Give the extent of all Plasmodium falciparum-infected red blood cells.
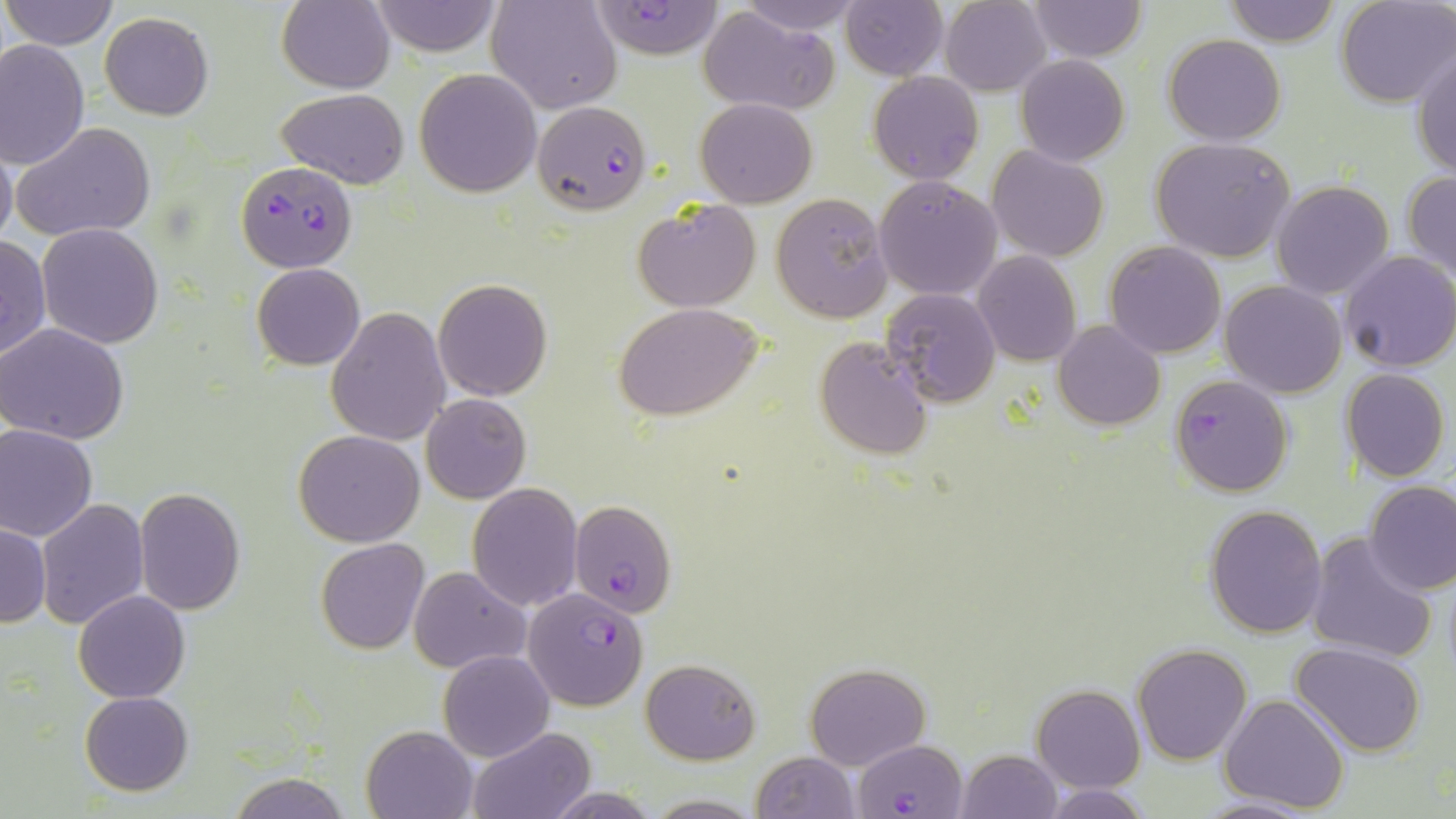

Approximate bounding boxes as (x1,y1)-(x2,y2) corner pairs in pixels.
Plasmodium falciparum-infected red blood cells: (595,0)-(724,61), (530,100)-(652,214), (236,161)-(356,273), (1169,373)-(1294,496), (570,501)-(677,617), (523,587)-(649,711), (855,737)-(971,818).

slide-level diagnosis = Plasmodium falciparum
uninfected red blood cell locations = approximate bounding boxes as (x1,y1)-(x2,y2) corner pairs in pixels: (2,0)-(118,51), (278,0)-(396,93), (487,0)-(623,115), (735,0)-(866,35), (841,0)-(949,80), (940,0)-(1051,95), (1025,0)-(1147,62), (1222,0)-(1342,47), (370,1)-(502,57), (1336,1)-(1454,107), (697,6)-(840,116), (100,12)-(214,120), (1163,34)-(1286,146), (0,39)-(91,172), (1411,47)-(1456,182), (1015,55)-(1131,166), (415,69)-(541,195), (867,71)-(983,184), (278,88)-(408,189), (696,98)-(816,207), (12,122)-(156,242), (0,136)-(17,255), (1151,137)-(1296,262), (987,146)-(1110,262), (1402,173)-(1456,282), (874,177)-(1003,300), (1271,180)-(1395,299), (771,193)-(892,322), (633,198)-(762,312), (38,224)-(164,348), (0,233)-(50,364), (1103,240)-(1229,358), (1336,249)-(1456,372), (973,250)-(1081,366), (253,264)-(365,370), (433,279)-(551,402), (1220,281)-(1347,398), (880,288)-(1001,406), (614,303)-(765,422), (327,308)-(451,447), (1053,320)-(1166,431), (2,323)-(130,444), (814,336)-(932,461), (1341,369)-(1449,482), (422,393)-(531,503), (0,424)-(98,541), (294,429)-(425,547), (1364,481)-(1456,595), (467,483)-(582,611), (135,488)-(245,613), (37,499)-(151,630), (1205,503)-(1329,637), (1,523)-(51,627), (1305,531)-(1438,667), (316,539)-(429,655), (408,566)-(529,674), (74,590)-(190,704), (1290,641)-(1428,756), (1133,643)-(1252,765), (439,649)-(554,762), (640,658)-(760,765), (805,662)-(930,769), (1032,683)-(1145,793), (80,692)-(193,795), (1219,693)-(1351,811), (361,725)-(476,819), (468,728)-(594,818), (957,749)-(1062,819), (751,751)-(860,819), (228,772)-(349,818), (1040,783)-(1152,818), (540,788)-(666,818), (642,795)-(765,817), (1194,795)-(1316,818)
preparation = thin blood smear
image size = 1456×819 pixels
magnification = 1000x
field of view = single
modality = optical microscopy
stain = May-Grünwald-Giemsa